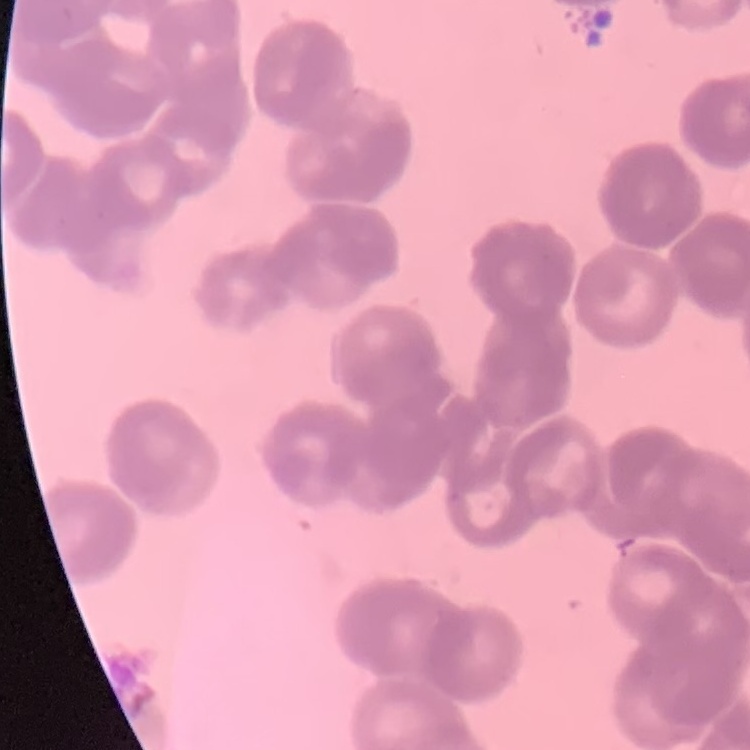 The erythrocytes exhibit rouleaux formation. Thin peripheral smear. One tile cut from a larger photomicrograph. Field's or Giemsa stain.